Describe the morphology of the erythrocytes.
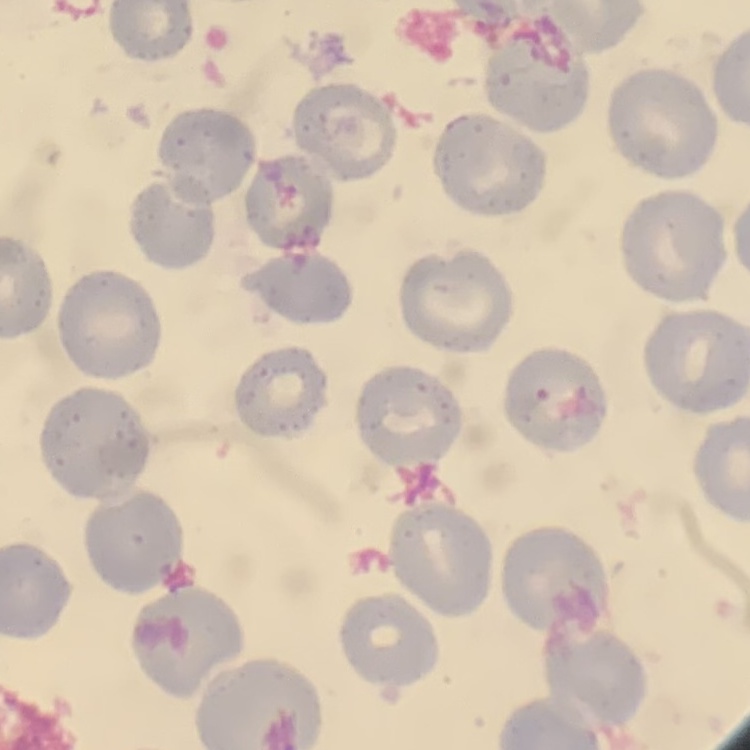
They show no rouleaux formation.

Stained with either Field's or Giemsa. Square crop of a larger photomicrograph. Thin peripheral smear.